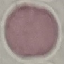

Summary:
  - Result: no malaria parasites seen
  - Stain: Giemsa
  - Preparation: thin blood film
  - Capture: smartphone through the microscope eyepiece
  - Image type: automatically extracted cell patch, resized to 64 × 64 pixels